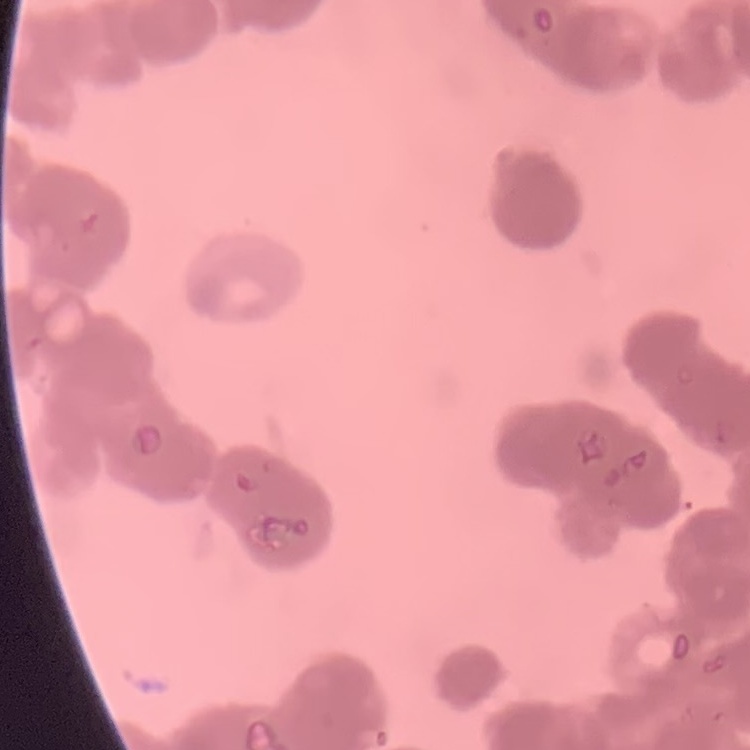

Summary:
  - Red blood cell morphology: rouleaux formation
  - Preparation: thin peripheral smear
  - Image type: one tile cut from a larger photomicrograph
  - Stain: Field's or Giemsa